Give the extent of all Plasmodium ovale-infected red blood cells.
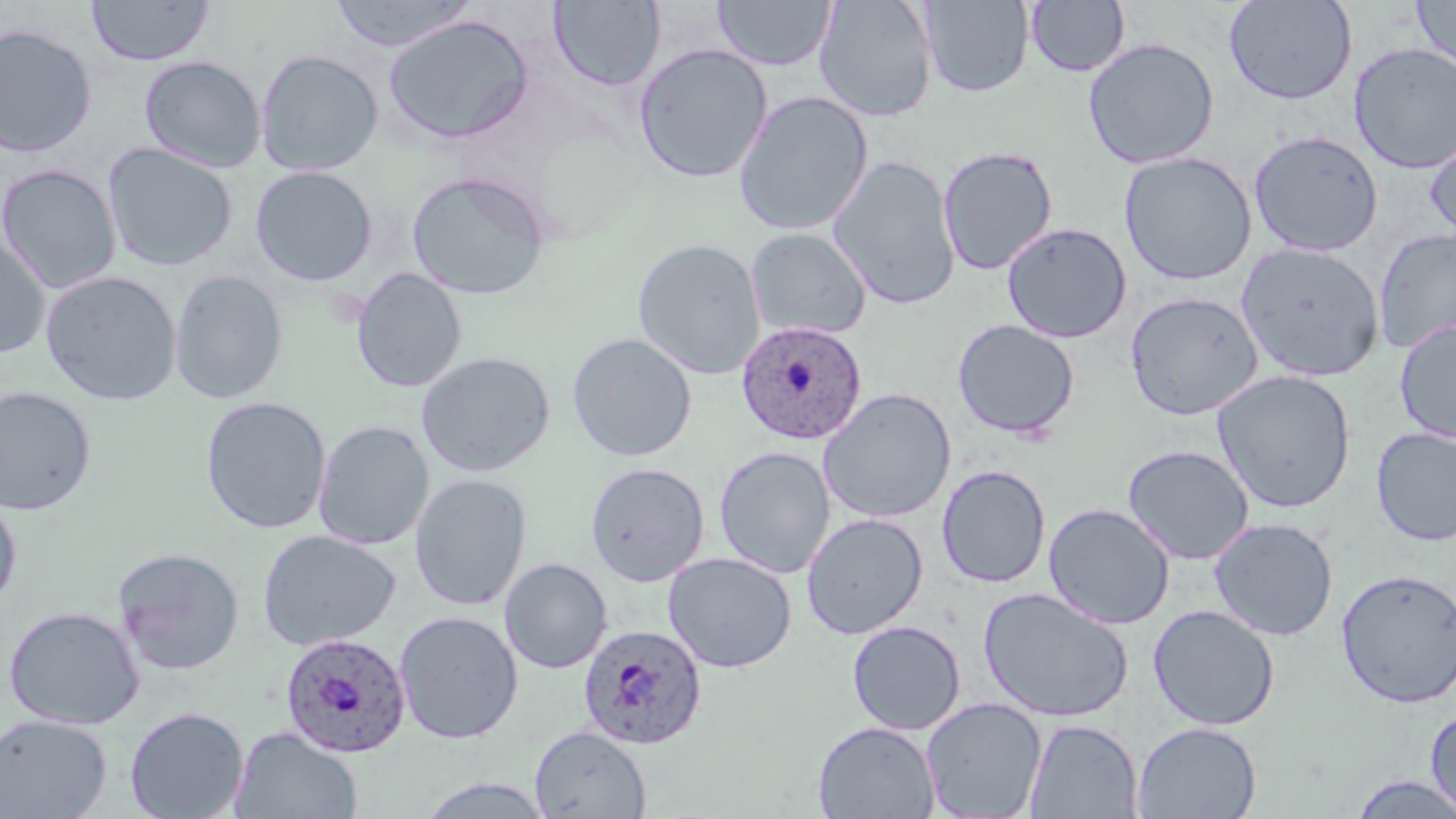

Approximate bounding boxes as [x1, y1, x2, y2] in pixels.
Plasmodium ovale-infected red blood cells: [736, 320, 867, 445], [578, 623, 706, 750], [279, 632, 411, 758].

Summary:
  - Uninfected red blood cell locations: [87, 0, 214, 66], [329, 0, 475, 52], [549, 0, 665, 90], [814, 0, 938, 123], [919, 0, 1033, 97], [1223, 0, 1358, 105], [1410, 0, 1456, 75], [713, 1, 836, 71], [1025, 1, 1129, 76], [383, 14, 534, 145], [0, 24, 97, 157], [1082, 37, 1220, 169], [633, 43, 773, 184], [1349, 43, 1456, 174], [255, 49, 382, 176], [139, 56, 266, 173], [733, 91, 873, 237], [1248, 131, 1383, 256], [1426, 133, 1456, 246], [102, 143, 237, 271], [937, 145, 1059, 275], [1119, 152, 1257, 286], [827, 155, 962, 310], [0, 165, 121, 293], [250, 166, 377, 286], [406, 170, 550, 300], [1001, 222, 1132, 343], [1373, 226, 1456, 356], [745, 227, 872, 341], [0, 236, 50, 360], [632, 238, 766, 379], [1236, 242, 1385, 381], [350, 267, 467, 393], [40, 271, 182, 406], [169, 271, 287, 404], [1125, 291, 1264, 420], [952, 319, 1080, 439], [1394, 319, 1456, 444], [567, 332, 698, 462], [416, 351, 556, 476], [1212, 370, 1357, 513], [0, 385, 98, 516], [817, 387, 957, 524], [200, 396, 332, 534], [314, 420, 434, 550], [1370, 427, 1456, 547], [1122, 444, 1255, 564], [714, 446, 835, 578], [585, 461, 710, 586], [936, 464, 1051, 588], [410, 473, 532, 610], [0, 493, 22, 608], [1043, 502, 1176, 629], [801, 512, 928, 639], [1209, 517, 1339, 641], [257, 529, 401, 651], [111, 546, 245, 676], [663, 551, 797, 673], [499, 558, 613, 674], [1336, 568, 1456, 708], [978, 586, 1134, 723], [1148, 604, 1281, 731], [3, 605, 145, 730], [394, 611, 523, 744], [847, 621, 965, 735], [921, 696, 1046, 818], [124, 706, 250, 818], [1425, 708, 1456, 815], [0, 714, 113, 819], [1023, 718, 1143, 818], [813, 721, 940, 818], [1131, 722, 1262, 819], [230, 726, 363, 818], [530, 726, 651, 818], [1345, 773, 1456, 818], [415, 776, 557, 819]
  - Slide-level diagnosis: Plasmodium ovale
  - Preparation: thin blood film
  - Magnification: 1000x
  - Field of view: single
  - Modality: light microscopy
  - Image size: 1456×819 pixels
  - Stain: May-Grünwald-Giemsa